Locate and identify every blood parasite.
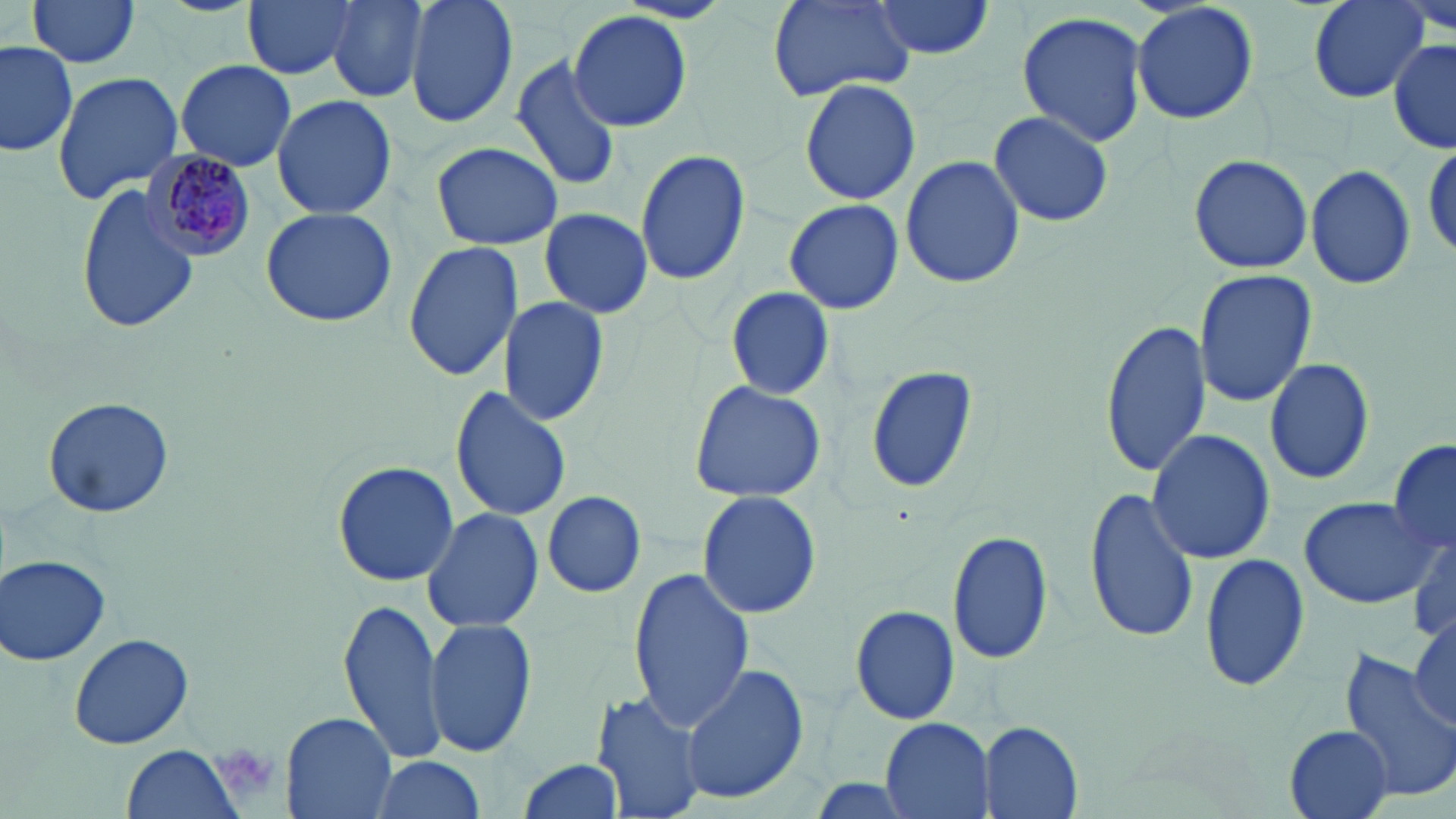

Approximate bounding boxes as (x1,y1)-(x2,y2) corner pairs in pixels.
Plasmodium malariae-infected red blood cells: (144,149)-(255,260).
No Plasmodium falciparum, Plasmodium ovale, Plasmodium vivax, Babesia divergens, or Trypanosoma brucei observed.

slide-level diagnosis = Plasmodium malariae
stain = May-Grünwald-Giemsa
image size = 1456×819 pixels
modality = light microscopy
uninfected red blood cell locations = approximate bounding boxes as (x1,y1)-(x2,y2) corner pairs in pixels: (23,0)-(144,69), (241,0)-(360,82), (327,0)-(429,103), (405,0)-(518,130), (768,0)-(915,101), (869,0)-(995,60), (1130,0)-(1261,124), (1303,0)-(1433,102), (568,9)-(694,134), (1017,11)-(1147,147), (1389,37)-(1456,157), (1,39)-(79,159), (510,53)-(621,191), (175,60)-(296,170), (51,70)-(184,205), (798,79)-(921,204), (270,94)-(397,219), (988,109)-(1114,229), (1423,139)-(1455,263), (431,141)-(562,248), (635,148)-(750,288), (1188,153)-(1314,275), (899,154)-(1026,288), (1305,165)-(1417,289), (77,181)-(198,334), (783,198)-(904,315), (259,206)-(400,328), (539,209)-(653,318), (403,240)-(524,381), (1194,269)-(1317,405), (726,287)-(835,400), (497,295)-(611,428), (1101,318)-(1211,477), (1264,355)-(1376,485), (862,360)-(980,497), (688,379)-(828,502), (449,385)-(573,522), (43,395)-(174,518), (1146,429)-(1276,564), (1388,438)-(1456,558), (332,459)-(459,588), (1082,489)-(1200,644), (541,490)-(646,598), (698,491)-(821,619), (1298,498)-(1438,609), (421,507)-(545,633), (947,528)-(1053,665), (1410,538)-(1454,642), (1199,553)-(1311,691), (2,555)-(111,666), (627,566)-(756,733), (339,598)-(448,766), (850,605)-(958,724), (1410,612)-(1455,732), (423,617)-(536,759), (69,633)-(194,749), (1339,652)-(1456,805), (679,663)-(809,805), (591,688)-(707,819), (280,711)-(397,819), (879,719)-(994,817), (978,720)-(1083,819), (1284,725)-(1393,817), (121,745)-(246,819), (368,755)-(485,819), (513,757)-(623,818)
field of view = single
preparation = thin blood film
magnification = 1000x
platelet locations = approximate bounding boxes as (x1,y1)-(x2,y2) corner pairs in pixels: (211,740)-(283,803)